Point out every malaria parasite.
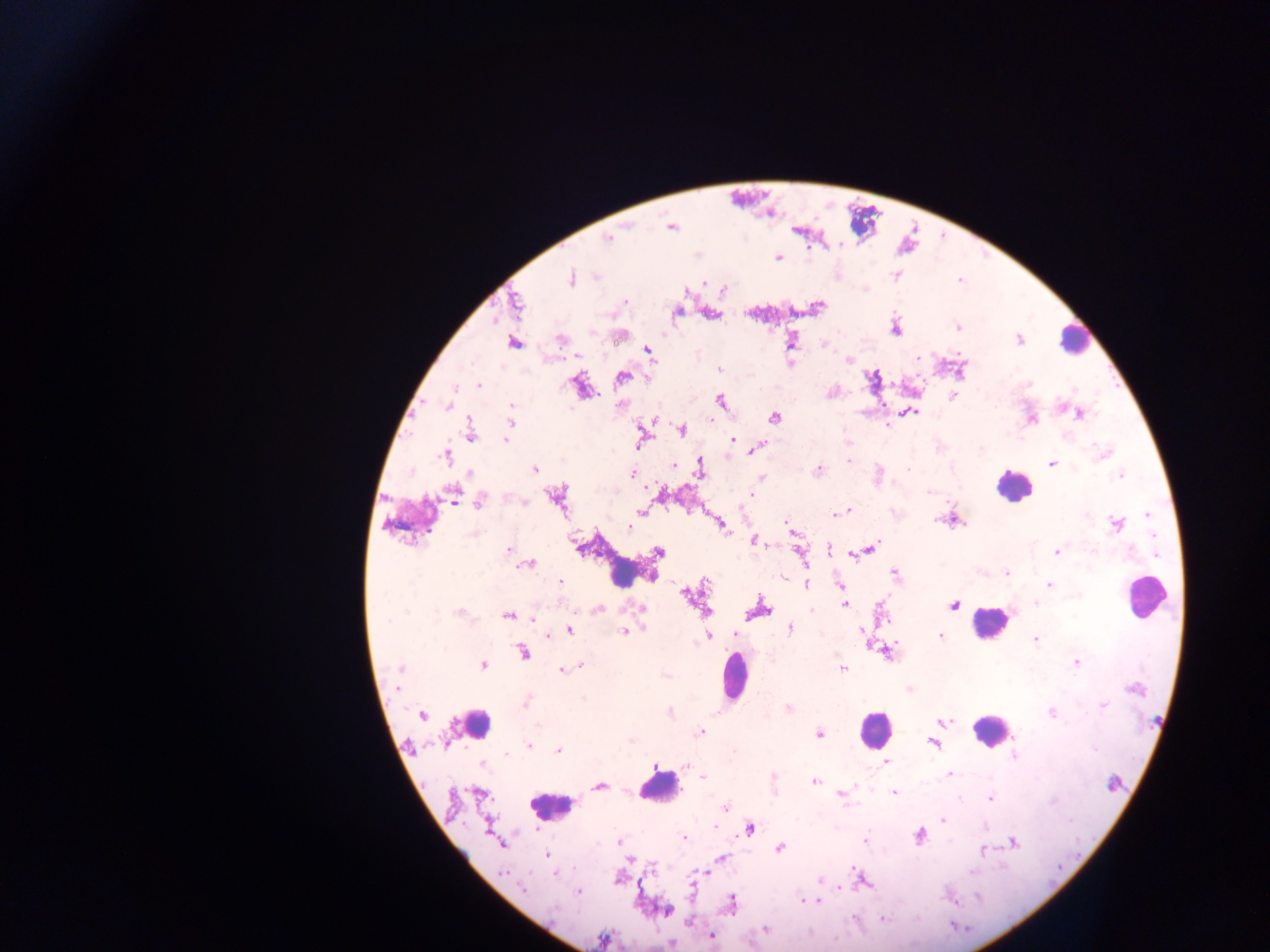

Approximate centers as [x, y] in pixels.
Malaria parasites: [671, 227], [608, 239], [839, 245], [778, 258], [596, 276], [571, 278], [704, 283], [515, 301], [624, 301], [819, 307], [957, 326], [896, 329], [561, 339], [1019, 340], [514, 342], [792, 342], [823, 345], [648, 351], [918, 358], [849, 360], [719, 369], [622, 376], [873, 376], [1029, 384], [479, 385], [953, 396], [720, 401], [448, 404], [511, 411], [912, 412], [1080, 415], [774, 418], [1032, 419], [511, 420], [652, 420], [887, 426], [682, 430], [470, 433], [505, 440], [732, 440], [757, 448], [1103, 453], [446, 456], [848, 461], [1052, 463], [674, 465], [535, 468], [701, 469], [820, 469], [908, 469], [470, 475], [632, 475], [1121, 475], [761, 478], [929, 492], [452, 494], [750, 494], [559, 497], [523, 501], [480, 502], [641, 511], [847, 511], [837, 514], [1149, 515], [936, 521], [959, 522], [1116, 524], [788, 525], [722, 526], [629, 527], [474, 533], [755, 541], [871, 548], [829, 549], [508, 550], [658, 552], [800, 553], [1057, 553], [853, 554], [528, 563], [894, 573], [1006, 573], [652, 575], [560, 581], [706, 583], [806, 583], [1050, 584], [840, 585], [686, 595], [844, 604], [1036, 604], [954, 605], [760, 607], [598, 609], [641, 609], [706, 612], [460, 613], [507, 616], [534, 618], [789, 629], [569, 630], [862, 631], [624, 632], [735, 634], [546, 636], [940, 636], [708, 637], [1036, 639], [524, 652], [1077, 662], [482, 665], [581, 666], [400, 668], [843, 668], [563, 670], [397, 689], [1134, 689], [583, 699], [525, 702], [1103, 705], [788, 707], [1051, 713], [422, 715], [944, 721], [700, 732], [820, 734], [934, 743], [529, 746], [558, 751], [507, 755], [1015, 756], [887, 762], [483, 765], [656, 766], [949, 774], [703, 777], [774, 777], [816, 782], [600, 786], [894, 792], [481, 794], [841, 795], [989, 797], [726, 808], [943, 819], [716, 826], [750, 829], [920, 836], [683, 838], [865, 840], [620, 841], [1014, 843], [501, 844], [780, 848], [983, 851], [547, 854], [723, 858], [630, 860], [654, 867], [503, 873], [555, 874], [862, 879], [820, 881], [693, 887], [524, 889], [578, 892], [950, 900], [804, 902], [818, 902], [731, 904], [667, 911], [884, 920], [766, 929], [711, 937], [601, 940].

Leukocyte locations: [1075, 338], [1012, 487], [620, 569], [1145, 597], [988, 622], [735, 677], [475, 723], [874, 728], [989, 730], [660, 788], [552, 806]. Thick blood smear. Image is 1270×952 pixels. Sample from Ghana. One field of view. Mobile-phone photograph taken through the microscope.